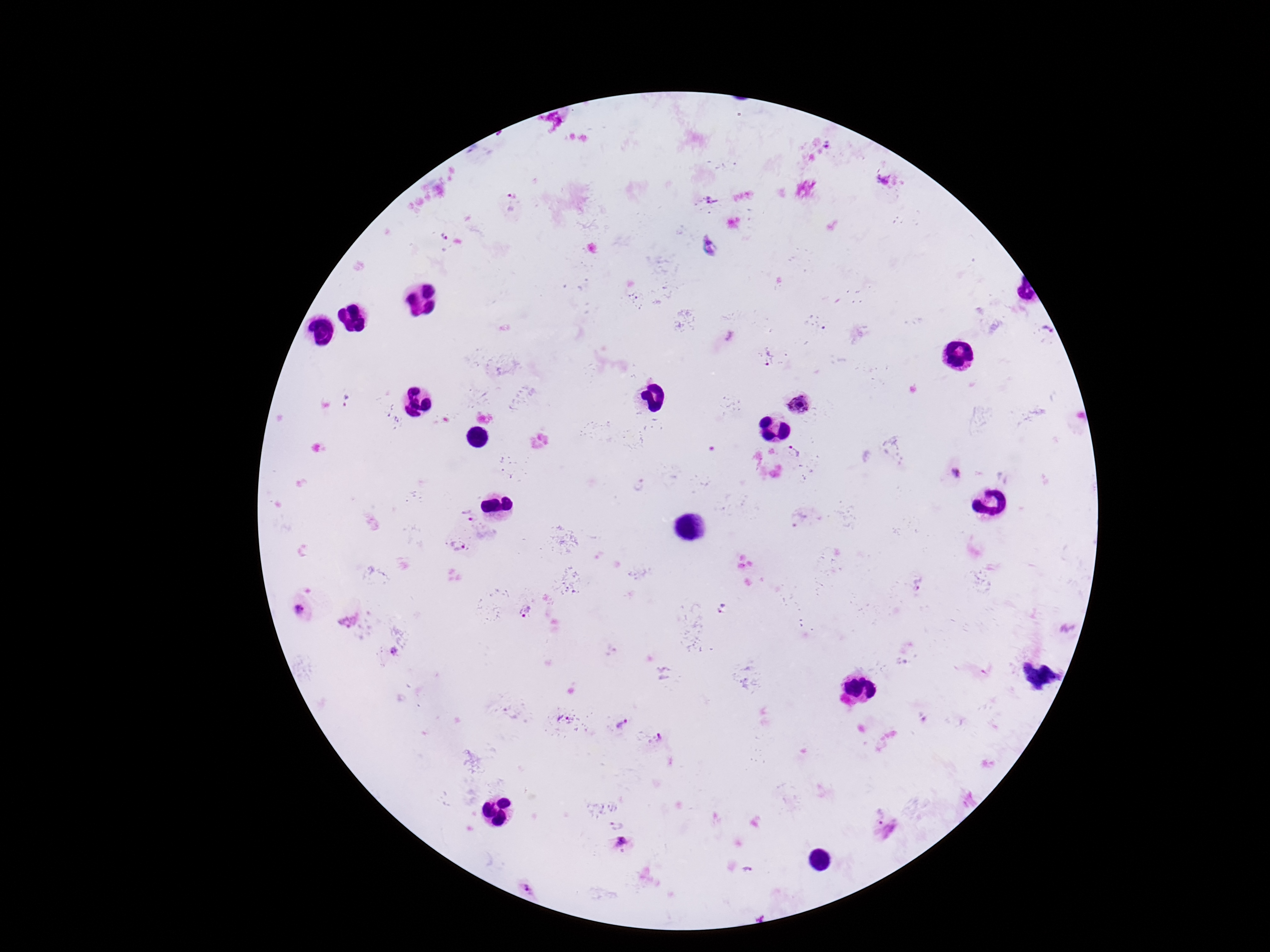

Approximate object centers, in pixels from the top-left corner.
Summary:
  - Plasmodium parasite locations: (x=713, y=199), (x=512, y=203), (x=443, y=237), (x=710, y=246), (x=1044, y=331), (x=770, y=360), (x=346, y=402), (x=800, y=404), (x=794, y=454), (x=956, y=474), (x=639, y=485), (x=468, y=517), (x=458, y=546), (x=918, y=584), (x=299, y=610), (x=525, y=612), (x=347, y=621), (x=395, y=652), (x=563, y=718), (x=622, y=724), (x=658, y=737), (x=879, y=814), (x=616, y=824), (x=623, y=842), (x=528, y=889)
  - Magnification: 100x
  - Image size: 1270×952 pixels
  - Field of view: one from this slide
  - Patient malaria status: infected
  - Preparation: thick blood smear
  - Capture: smartphone camera through the microscope eyepiece
  - Stain: Giemsa